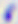 Micrograph. Captured at 400x magnification. Toxoplasma gondii is shown.